Give a bounding box for every leukocyte visible.
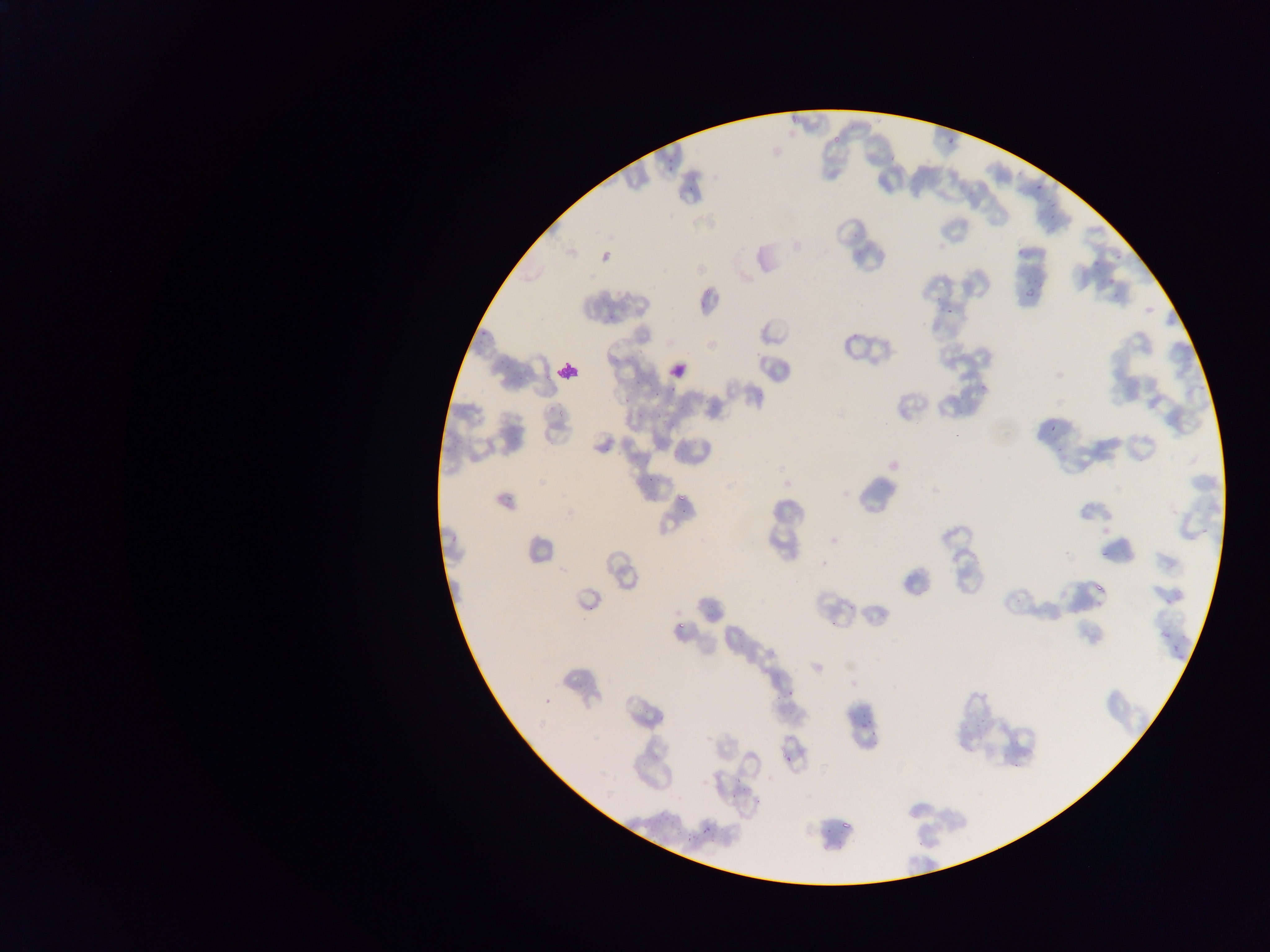
Approximate bounding boxes as (left, top, right, bottom) in pixels.
Leukocytes: (663, 356, 689, 381), (552, 358, 580, 383).

Malaria parasite locations: (946, 136, 954, 145), (667, 165, 675, 174), (1034, 185, 1042, 191), (1022, 285, 1034, 302), (979, 385, 987, 393), (1048, 417, 1055, 435), (677, 493, 685, 500), (1097, 550, 1109, 559), (673, 623, 681, 632), (788, 682, 802, 701), (857, 711, 874, 734), (783, 751, 797, 767), (749, 795, 767, 805), (700, 826, 711, 834), (681, 831, 698, 844) | approximate (x, y) pixel centers of objects too small to bound: (948, 311). Sample from Ghana. Thin blood smear. Single field of view. Image is 1270×952 pixels. Mobile-phone photograph taken through the microscope.